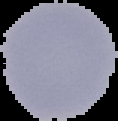 Image is 118×121 pixels. Malaria status: uninfected. Cell region segmented out of the field of view; the surrounding area is masked to black. From a thin blood film.